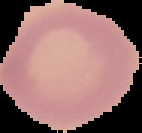

Summary:
  - Image size: 142×133 pixels
  - Preparation: thin blood film
  - Malaria status: uninfected
  - Image type: cell region segmented out of the field of view; surrounding area masked to black